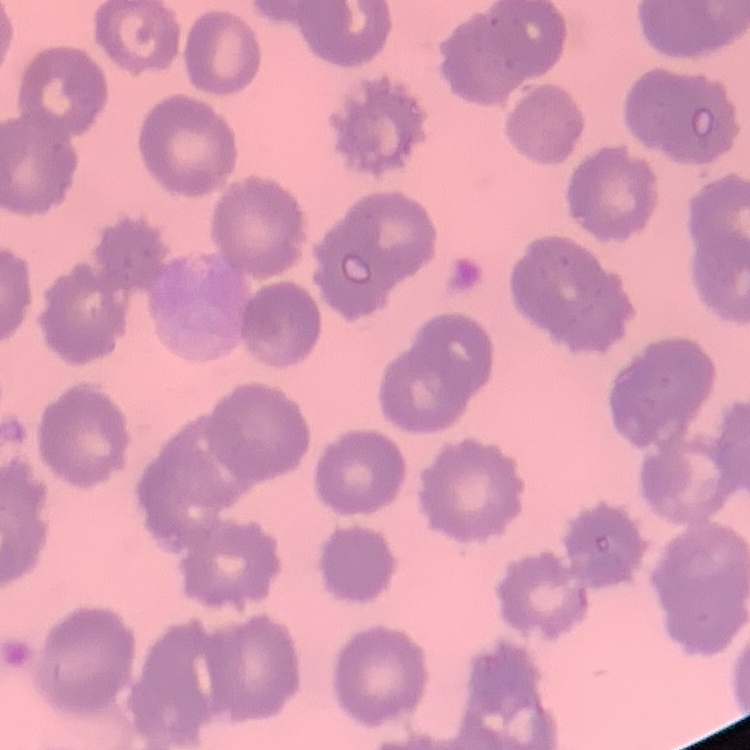

{
  "red_blood_cell_morphology": "no rouleaux formation",
  "preparation": "thin blood smear",
  "stain": "Field's or Giemsa",
  "image_type": "one tile cut from a larger photomicrograph"
}